Locate every P. falciparum parasite and identify its life-cycle stage.
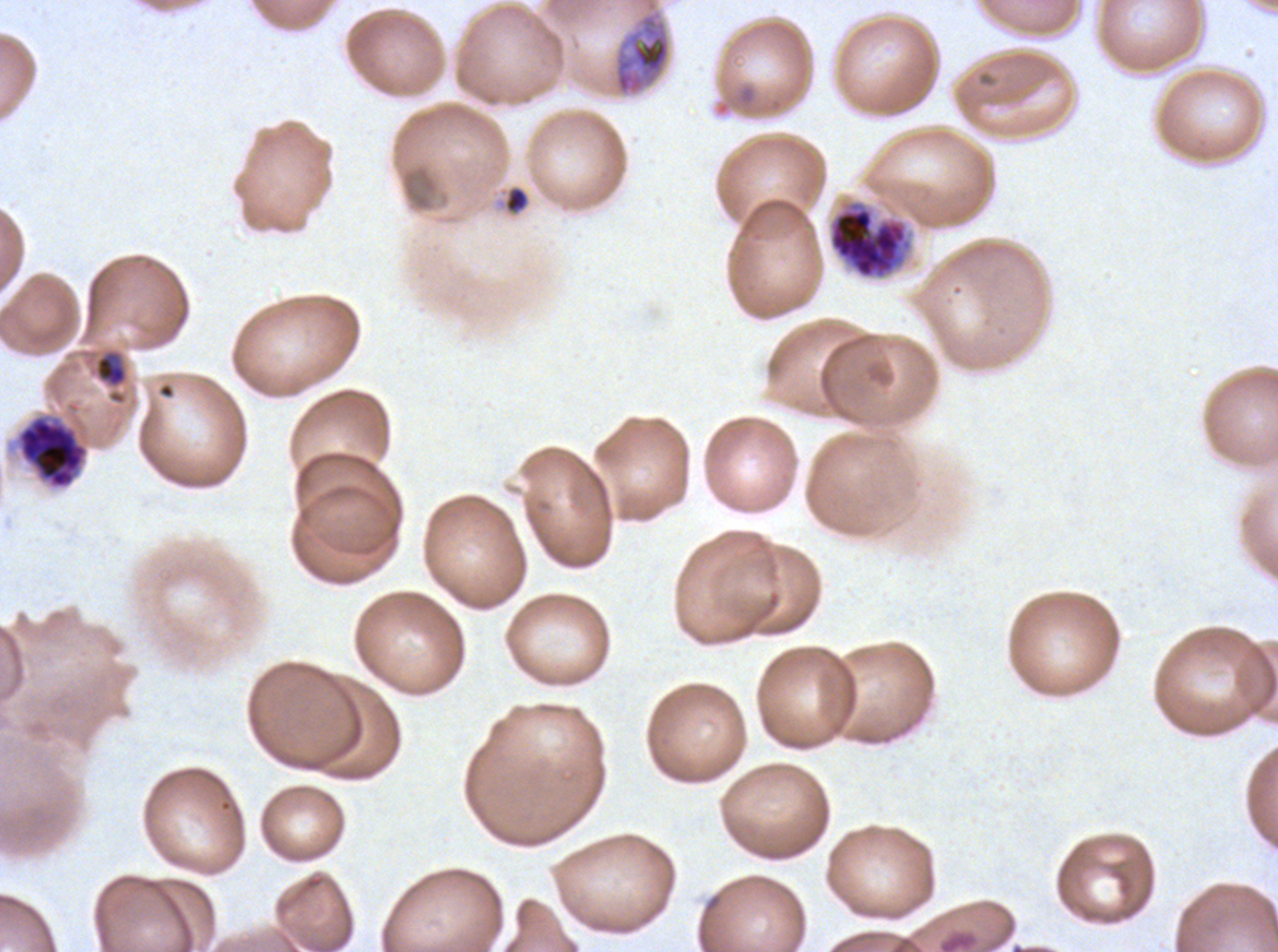

Approximate bounding boxes as [x1, y1, x2, y2] in pixels.
Late-ring/early-trophozoite forms: [503, 185, 530, 214], [94, 351, 128, 387].
Late trophozoites: [613, 0, 671, 96].
Late schizonts: [827, 199, 914, 281], [17, 416, 88, 489].
No rings, mid trophozoites, early schizonts, segmenters, or gametocytes observed.

field_of_view: sub-image separated from a larger composite
image_size: 1278×952 pixels
life_cycle_stages_observed: late-ring/early-trophozoite, late trophozoite, late schizont
stain: Giemsa
specimen: ex-vivo P. falciparum culture from a patient in The Gambia, grown for 24 to 48 hours
preparation: thin blood film